Name the parasite shown.
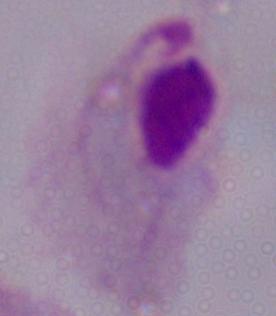
A trichomonad.

Summary:
  - Magnification: 1000x
  - Modality: photomicrograph